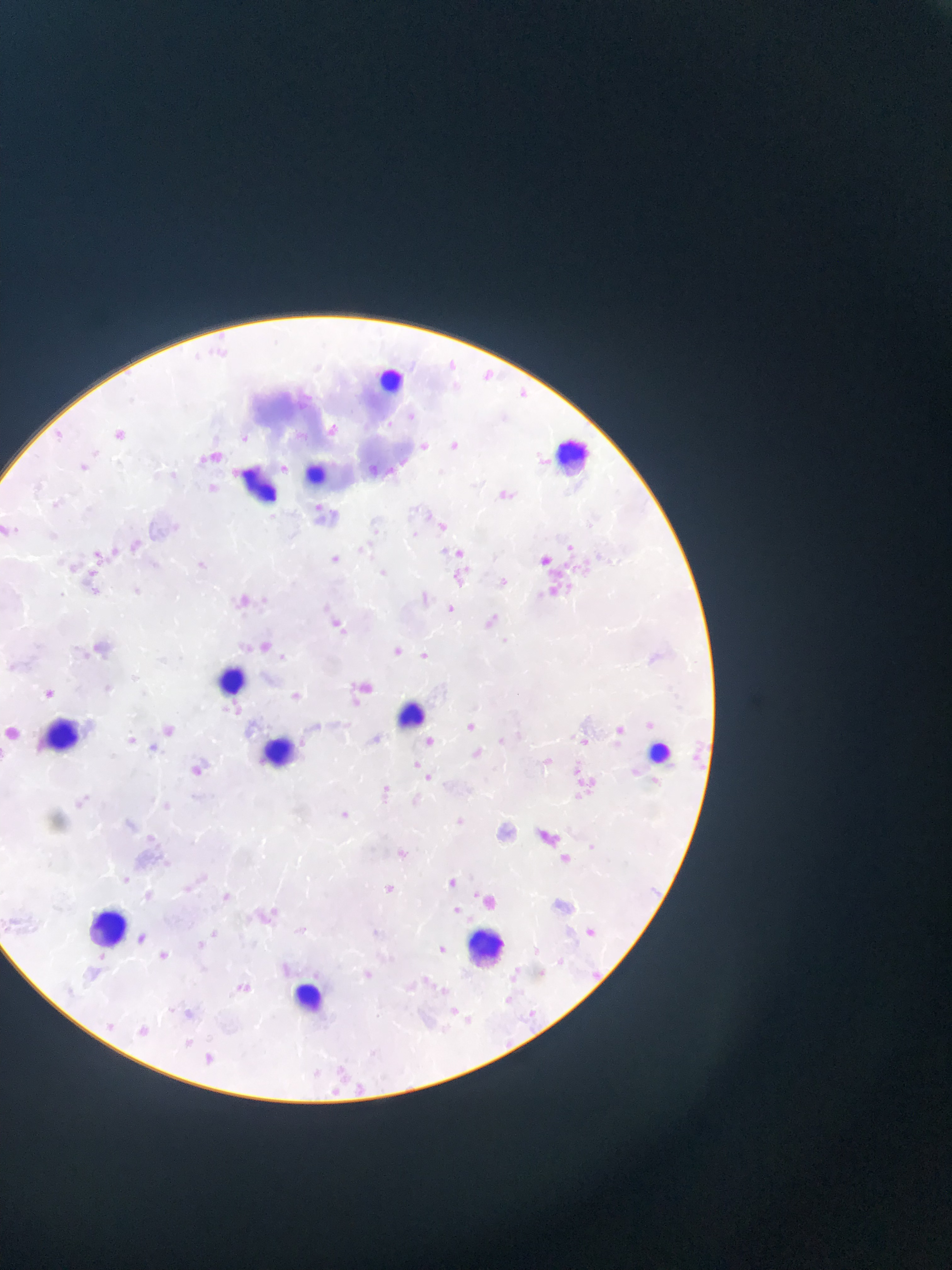 Approximate bounding boxes as (left, top, right, bottom) in pixels. Leukocyte locations: (382, 359, 420, 391), (545, 437, 592, 475), (305, 457, 331, 484), (237, 464, 277, 509), (221, 664, 267, 709), (389, 695, 425, 724), (37, 715, 75, 748), (640, 724, 688, 773), (253, 733, 305, 761), (88, 901, 129, 941), (459, 925, 507, 966), (459, 953, 553, 957), (291, 970, 338, 1022). Malaria parasite locations: (443, 357, 461, 376), (480, 366, 498, 385), (514, 384, 532, 401), (284, 385, 324, 416), (318, 411, 356, 446), (448, 430, 473, 450), (109, 431, 129, 446), (413, 433, 441, 460), (208, 448, 228, 463), (367, 460, 387, 476), (496, 476, 523, 507), (309, 496, 328, 522), (426, 504, 451, 525), (562, 529, 593, 549), (126, 530, 152, 558), (538, 538, 563, 563), (359, 542, 368, 555), (94, 544, 122, 572), (451, 545, 476, 569), (326, 552, 344, 568), (371, 559, 387, 578), (554, 561, 579, 581), (444, 567, 471, 588), (89, 573, 114, 597), (496, 574, 512, 589), (555, 579, 575, 598), (234, 587, 264, 618), (443, 602, 459, 617), (485, 610, 498, 625), (326, 613, 350, 637), (91, 633, 114, 657), (258, 634, 272, 647), (389, 644, 407, 661), (415, 647, 432, 663), (357, 676, 376, 695), (283, 683, 301, 704), (39, 684, 59, 702), (338, 712, 354, 739), (609, 716, 639, 748), (160, 718, 175, 737), (458, 720, 490, 740), (9, 723, 25, 745), (368, 724, 382, 745), (573, 730, 593, 749), (123, 733, 139, 748), (409, 734, 434, 752), (464, 746, 496, 771), (541, 753, 569, 772), (192, 758, 217, 784), (411, 758, 433, 784), (578, 768, 596, 804), (364, 781, 384, 803), (79, 791, 97, 809), (156, 793, 177, 815), (330, 799, 362, 824), (450, 812, 471, 831), (541, 827, 577, 855), (142, 828, 168, 858), (391, 844, 412, 863), (118, 872, 134, 888), (443, 873, 461, 891), (178, 880, 196, 898), (557, 880, 581, 906), (378, 881, 399, 899), (139, 886, 157, 905), (473, 887, 505, 908), (217, 889, 234, 905), (447, 901, 465, 918), (253, 909, 273, 923), (21, 914, 56, 937), (579, 921, 602, 942), (366, 922, 396, 943), (136, 923, 149, 944), (205, 928, 222, 942), (192, 936, 210, 953), (433, 941, 451, 958), (89, 946, 107, 969), (154, 947, 173, 965), (584, 965, 606, 987), (403, 968, 424, 996), (230, 978, 252, 999), (445, 995, 467, 1020), (175, 1005, 196, 1022), (522, 1005, 541, 1024), (101, 1018, 119, 1036), (134, 1022, 154, 1040), (180, 1034, 196, 1050), (197, 1048, 221, 1068), (331, 1056, 347, 1077), (321, 1074, 347, 1099), (344, 1079, 369, 1098). Image is 952×1270 pixels. Photographed through a microscope with a mobile-phone camera. Sample from Ghana. Thin blood film. Single field of view.